Classify this cell by malaria status.
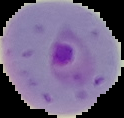
Parasitized.

From a thin blood smear. Segmented cell region on a black background. Image is 124×118 pixels.